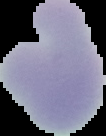

Summary:
  - Result: no malaria parasites detected
  - Image type: cell region segmented out of the field of view; surrounding area masked to black
  - Image size: 106×136 pixels
  - Preparation: thin blood film